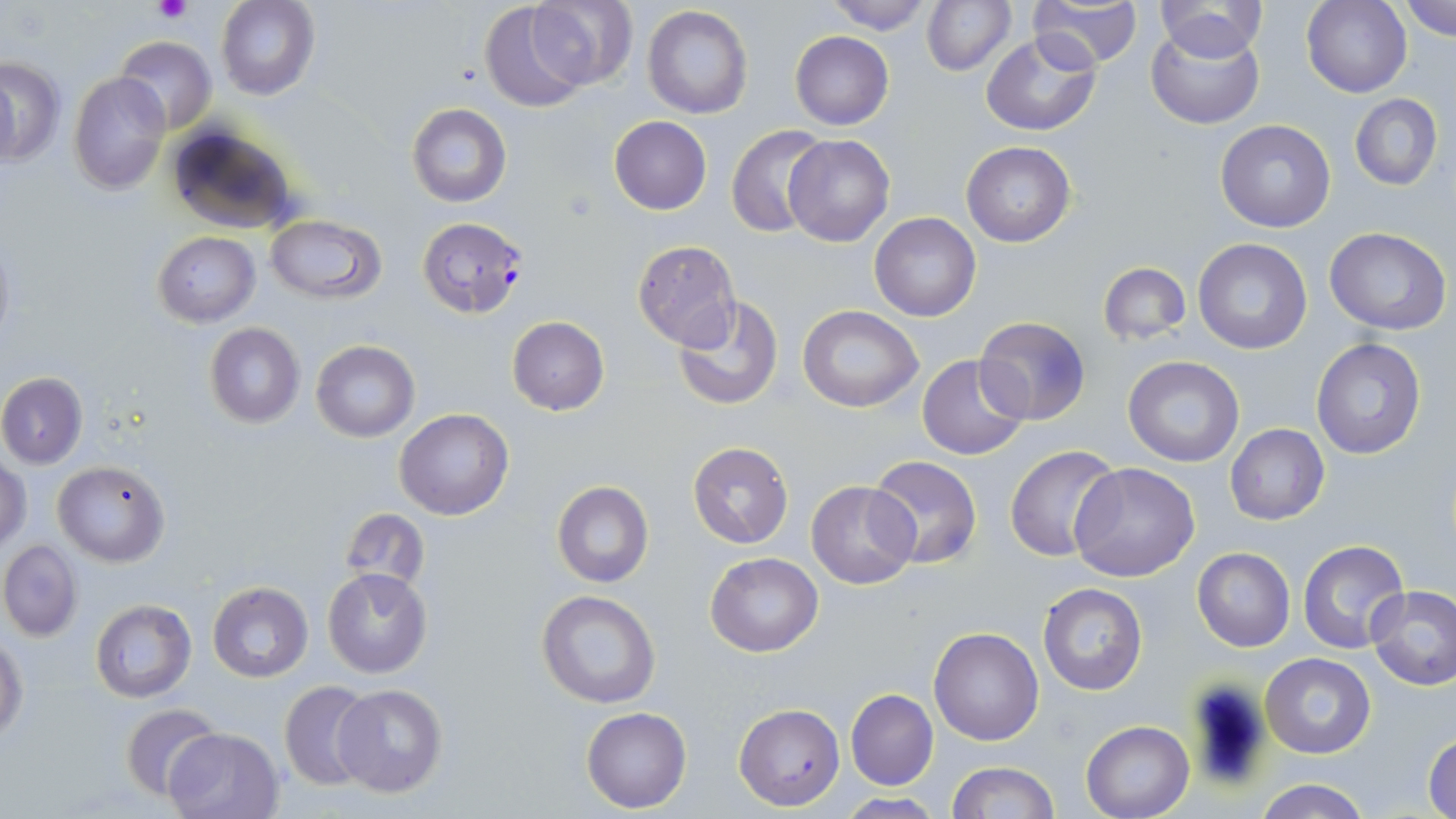

Summary:
  - Coordinate format: approximate bounding boxes as [x1, y1, x2, y2] in pixels
  - Uninfected red blood cell locations: [216, 0, 319, 100], [821, 0, 940, 35], [921, 0, 1016, 75], [1028, 0, 1143, 71], [1401, 0, 1456, 40], [529, 1, 638, 90], [1153, 1, 1267, 63], [1303, 1, 1413, 98], [478, 2, 590, 113], [642, 5, 752, 118], [1146, 23, 1264, 130], [790, 31, 893, 129], [980, 31, 1101, 136], [115, 35, 216, 133], [0, 56, 65, 167], [0, 65, 20, 171], [68, 73, 169, 193], [1349, 94, 1443, 191], [406, 103, 512, 207], [608, 116, 711, 215], [1215, 120, 1335, 233], [164, 122, 301, 236], [728, 124, 832, 238], [785, 135, 893, 245], [961, 141, 1076, 248], [870, 212, 981, 321], [264, 216, 386, 303], [1324, 228, 1451, 334], [151, 232, 260, 326], [631, 239, 743, 350], [1192, 239, 1311, 353], [1097, 260, 1192, 345], [674, 296, 782, 412], [796, 306, 924, 412], [506, 316, 609, 415], [975, 316, 1091, 424], [203, 322, 306, 428], [1311, 338, 1427, 460], [310, 340, 420, 441], [916, 354, 1029, 459], [1123, 355, 1245, 466], [0, 372, 87, 469], [395, 408, 514, 521], [1225, 424, 1329, 526], [687, 441, 793, 549], [1004, 445, 1124, 563], [867, 455, 982, 568], [1, 456, 31, 553], [53, 460, 170, 567], [1071, 462, 1200, 583], [805, 480, 919, 589], [551, 481, 654, 587], [341, 510, 429, 590], [1297, 538, 1411, 654], [0, 539, 82, 642], [1192, 547, 1295, 651], [705, 553, 822, 657], [323, 567, 431, 677], [207, 581, 313, 683], [1038, 583, 1147, 697], [1366, 584, 1456, 691], [535, 590, 661, 709], [89, 599, 196, 702], [930, 626, 1043, 746], [0, 635, 27, 744], [1262, 654, 1376, 758], [279, 680, 374, 792], [334, 684, 448, 799], [845, 689, 938, 790], [119, 702, 224, 803], [733, 703, 844, 810], [582, 707, 692, 813], [1080, 719, 1197, 819], [164, 726, 286, 819], [1424, 734, 1456, 819], [946, 760, 1059, 818], [1253, 778, 1372, 819], [838, 795, 943, 818]
  - Platelet locations: [153, 0, 190, 22]
  - Plasmodium falciparum-infected red blood cell locations: [417, 217, 530, 319]
  - Slide-level diagnosis: Plasmodium falciparum
  - Image size: 1456×819 pixels
  - Magnification: 1000x
  - Preparation: thin blood film
  - Stain: May-Grünwald-Giemsa
  - Modality: optical microscopy
  - Field of view: one of a larger specimen